Assess this cell for malaria.
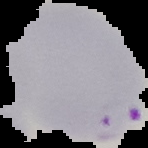

It is parasitized.

From a thin blood film. Image is 148×148 pixels. Segmented cell region on a black background.